Give the extent of all Plasmodium falciparum-infected red blood cells.
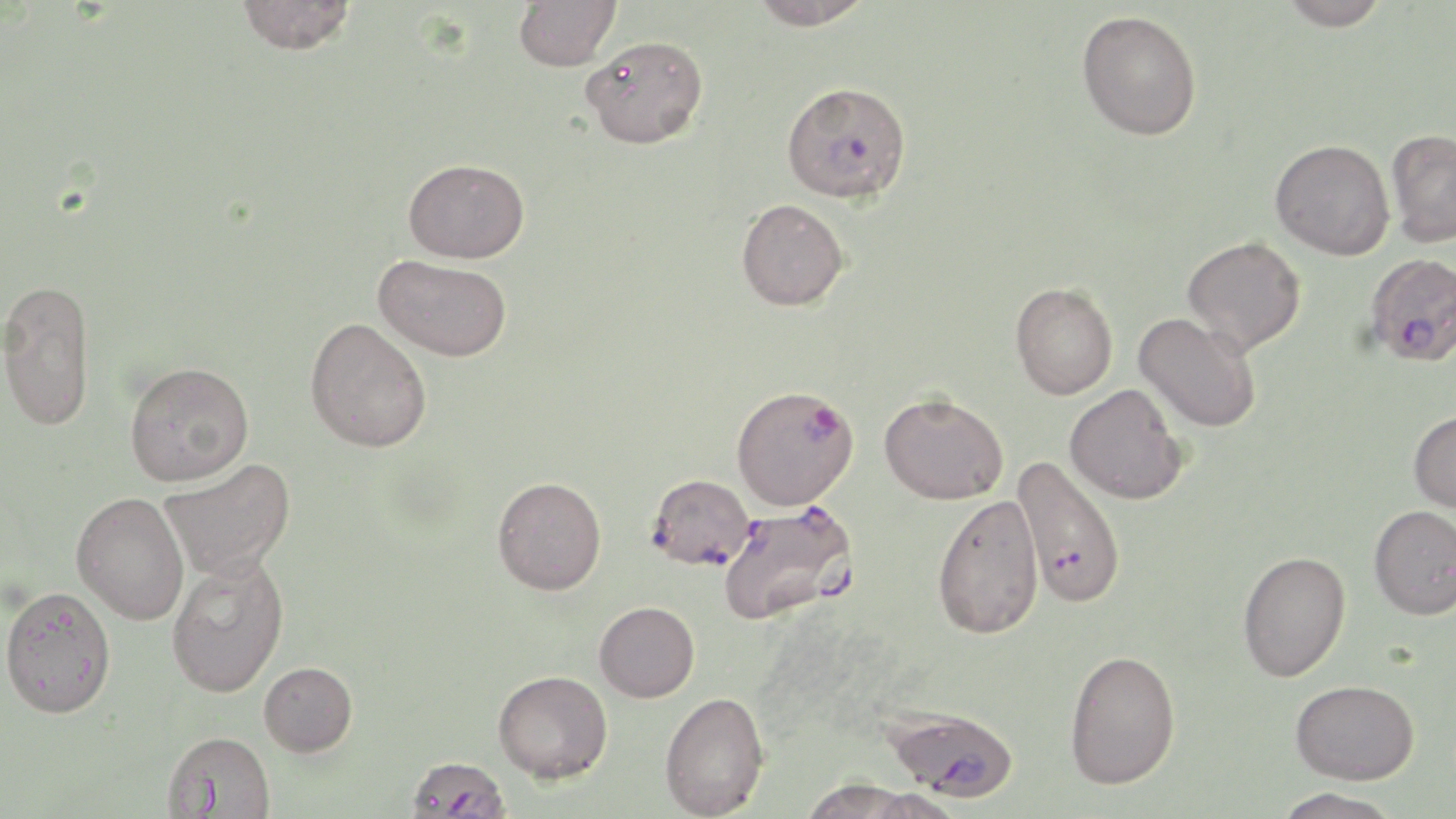
Approximate bounding boxes as (x1, y1, x2, y2) in pixels.
Plasmodium falciparum-infected red blood cells: (781, 81, 912, 204), (1364, 252, 1456, 367), (730, 386, 858, 510), (1013, 455, 1128, 608), (647, 474, 754, 570), (721, 503, 860, 626), (883, 704, 1020, 802), (405, 756, 511, 819).

Uninfected red blood cell locations: (235, 0, 356, 55), (513, 0, 621, 71), (748, 0, 876, 30), (1278, 0, 1391, 30), (1076, 9, 1202, 140), (580, 35, 708, 148), (1385, 128, 1456, 248), (1270, 139, 1394, 260), (403, 157, 529, 263), (736, 198, 849, 311), (1182, 236, 1306, 356), (374, 254, 512, 362), (0, 278, 96, 431), (1010, 282, 1118, 399), (1134, 313, 1261, 433), (305, 317, 432, 452), (124, 362, 253, 486), (1064, 382, 1187, 504), (879, 392, 1008, 504), (1408, 409, 1456, 514), (159, 458, 296, 581), (492, 476, 607, 594), (72, 491, 189, 624), (931, 494, 1045, 640), (1368, 504, 1456, 620), (1237, 550, 1351, 682), (166, 555, 289, 698), (1, 584, 117, 718), (594, 601, 699, 702), (1064, 648, 1181, 790), (259, 661, 358, 757), (493, 670, 612, 783), (1290, 678, 1419, 784), (659, 691, 770, 818), (163, 730, 276, 819), (799, 780, 952, 819), (1272, 787, 1405, 819). Slide-level diagnosis: Plasmodium falciparum. One field of a larger specimen. May-Grünwald-Giemsa stain. 1000x magnification. Thin blood smear. Image is 1456×819 pixels. Light microscopy.